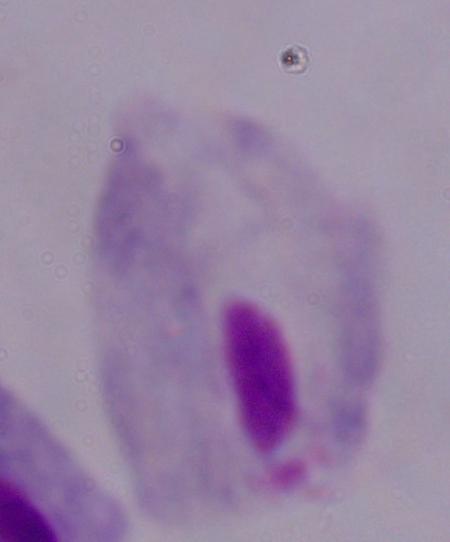
Summary:
  - Magnification: 1000x
  - Identification: trichomonad
  - Modality: photomicrograph